Give the extent of all Plasmodium vivax-infected red blood cells.
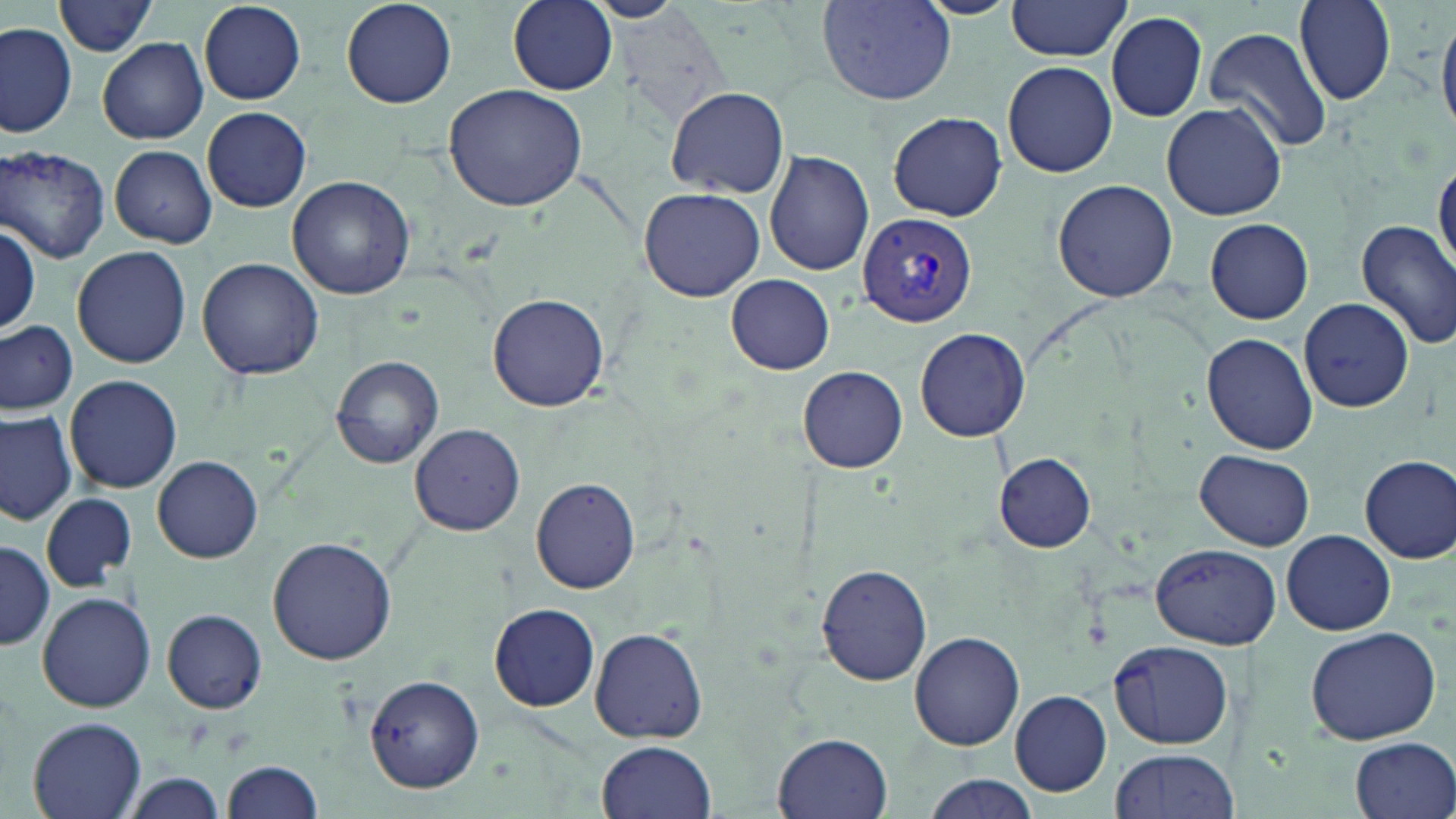

Approximate bounding boxes as named x1/y1/x2/y2 corners in pixels.
Plasmodium vivax-infected red blood cells: (x1=857, y1=212, x2=979, y2=328).

Summary:
  - Uninfected red blood cell locations: (x1=340, y1=0, x2=459, y2=108), (x1=508, y1=0, x2=618, y2=94), (x1=816, y1=0, x2=955, y2=105), (x1=1293, y1=0, x2=1396, y2=105), (x1=55, y1=1, x2=159, y2=57), (x1=197, y1=2, x2=308, y2=105), (x1=1003, y1=2, x2=1132, y2=63), (x1=1105, y1=12, x2=1208, y2=122), (x1=1438, y1=14, x2=1456, y2=135), (x1=0, y1=24, x2=77, y2=137), (x1=1204, y1=27, x2=1331, y2=152), (x1=97, y1=37, x2=208, y2=145), (x1=1002, y1=61, x2=1117, y2=178), (x1=444, y1=81, x2=590, y2=213), (x1=668, y1=87, x2=788, y2=200), (x1=1161, y1=101, x2=1287, y2=221), (x1=202, y1=107, x2=312, y2=212), (x1=887, y1=112, x2=1009, y2=221), (x1=109, y1=145, x2=217, y2=248), (x1=1, y1=146, x2=112, y2=262), (x1=764, y1=150, x2=876, y2=276), (x1=1434, y1=160, x2=1456, y2=275), (x1=287, y1=175, x2=417, y2=301), (x1=1052, y1=178, x2=1179, y2=302), (x1=639, y1=186, x2=766, y2=301), (x1=0, y1=219, x2=40, y2=336), (x1=1205, y1=219, x2=1314, y2=324), (x1=1355, y1=220, x2=1456, y2=349), (x1=72, y1=246, x2=192, y2=368), (x1=196, y1=257, x2=325, y2=380), (x1=725, y1=274, x2=836, y2=375), (x1=488, y1=292, x2=609, y2=412), (x1=1300, y1=298, x2=1415, y2=414), (x1=0, y1=318, x2=80, y2=414), (x1=915, y1=328, x2=1030, y2=441), (x1=1202, y1=332, x2=1318, y2=455), (x1=331, y1=356, x2=445, y2=469), (x1=799, y1=365, x2=908, y2=472), (x1=64, y1=374, x2=182, y2=495), (x1=0, y1=410, x2=78, y2=526), (x1=408, y1=423, x2=525, y2=536), (x1=1196, y1=450, x2=1314, y2=550), (x1=993, y1=453, x2=1095, y2=552), (x1=1359, y1=454, x2=1456, y2=562), (x1=152, y1=455, x2=263, y2=563), (x1=531, y1=477, x2=641, y2=593), (x1=41, y1=492, x2=136, y2=592), (x1=1283, y1=530, x2=1394, y2=635), (x1=267, y1=536, x2=398, y2=665), (x1=0, y1=539, x2=54, y2=653), (x1=1149, y1=543, x2=1279, y2=648), (x1=815, y1=563, x2=933, y2=686), (x1=36, y1=591, x2=155, y2=713), (x1=489, y1=604, x2=600, y2=712), (x1=161, y1=609, x2=267, y2=712), (x1=590, y1=626, x2=708, y2=744), (x1=1304, y1=626, x2=1444, y2=747), (x1=911, y1=632, x2=1025, y2=752), (x1=1107, y1=638, x2=1234, y2=749), (x1=365, y1=674, x2=483, y2=792), (x1=1008, y1=690, x2=1113, y2=798), (x1=26, y1=716, x2=147, y2=819), (x1=774, y1=731, x2=894, y2=819), (x1=1350, y1=736, x2=1456, y2=819), (x1=597, y1=741, x2=716, y2=819), (x1=1107, y1=748, x2=1239, y2=816), (x1=222, y1=761, x2=325, y2=818), (x1=121, y1=773, x2=225, y2=815), (x1=921, y1=775, x2=1039, y2=818)
  - Slide-level diagnosis: Plasmodium vivax
  - Stain: May-Grünwald-Giemsa
  - Field of view: single
  - Magnification: 1000x
  - Image size: 1456×819 pixels
  - Modality: optical microscopy
  - Preparation: thin blood film